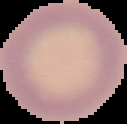

Summary:
  - Malaria status: uninfected
  - Image size: 127×124 pixels
  - Image type: cell region segmented out of the field of view; surrounding area masked to black
  - Preparation: thin blood film